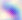
Summary:
  - Magnification: 400x
  - Identification: Toxoplasma gondii
  - Modality: micrograph